Classify this cell by malaria status.
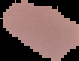
It is uninfected.

Image is 79×61 pixels. From a thin blood film. Segmented cell region on a black background.